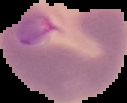
{
  "result": "negative for Plasmodium parasites",
  "image_type": "cell region segmented out of the field of view; surrounding area masked to black",
  "preparation": "thin blood film",
  "image_size": "127×103 pixels"
}